Point out each leukocyte.
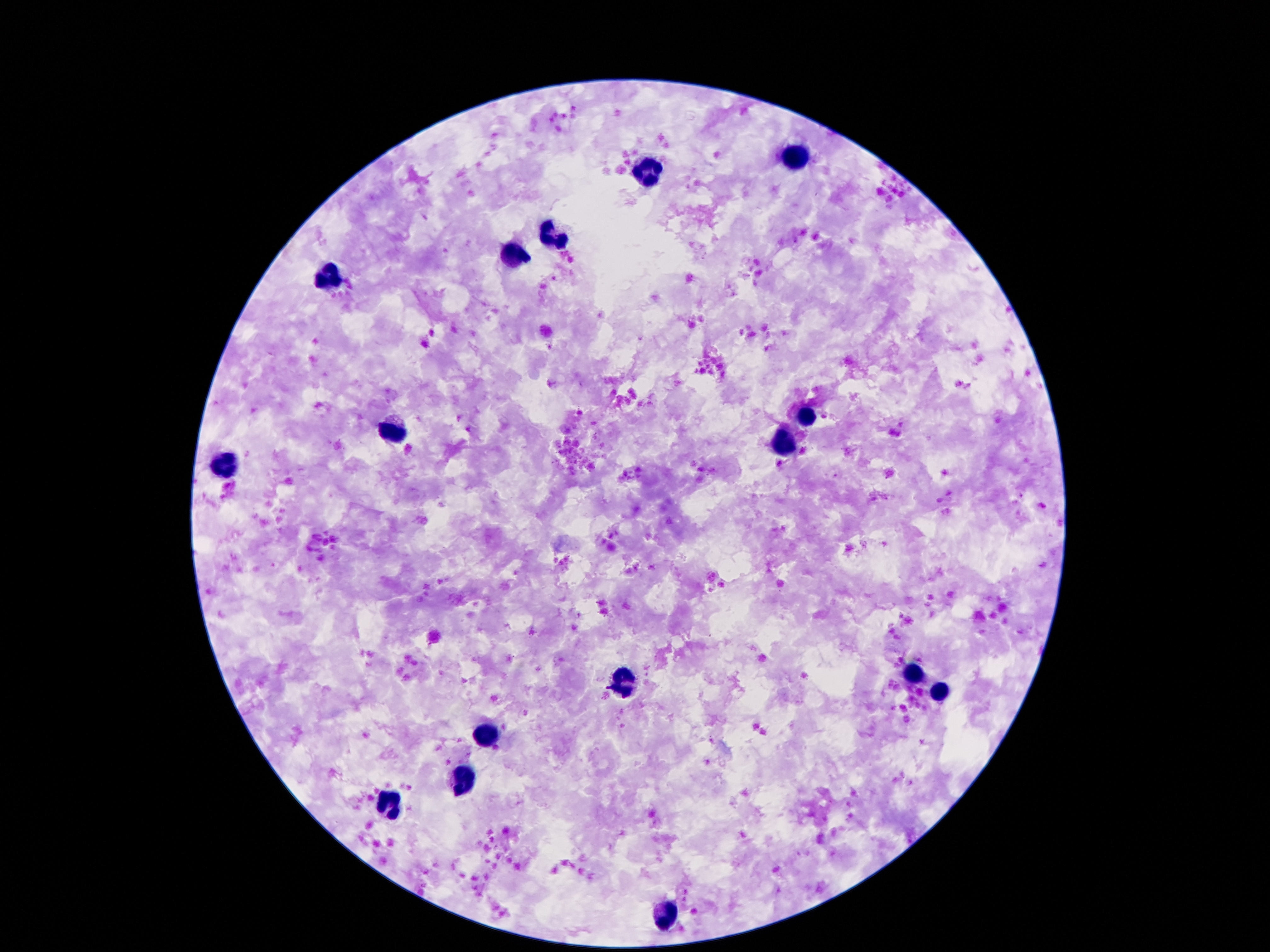

Approximate object centers, in pixels from the top-left corner.
Leukocytes: (x=794, y=156), (x=644, y=172), (x=551, y=234), (x=515, y=257), (x=327, y=279), (x=805, y=415), (x=391, y=430), (x=783, y=444), (x=223, y=468), (x=913, y=678), (x=626, y=680), (x=942, y=696), (x=484, y=735), (x=462, y=781), (x=387, y=806), (x=666, y=916).

preparation = thick blood smear
patient malaria status = uninfected
capture = smartphone camera through the microscope eyepiece
image size = 1270×952 pixels
stain = Giemsa
magnification = 100x
field of view = single